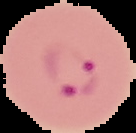

Summary:
  - Image size: 136×133 pixels
  - Preparation: thin blood smear
  - Result: malaria parasites detected
  - Image type: segmented cell region with the area outside set to black